Look for Plasmodium parasites.
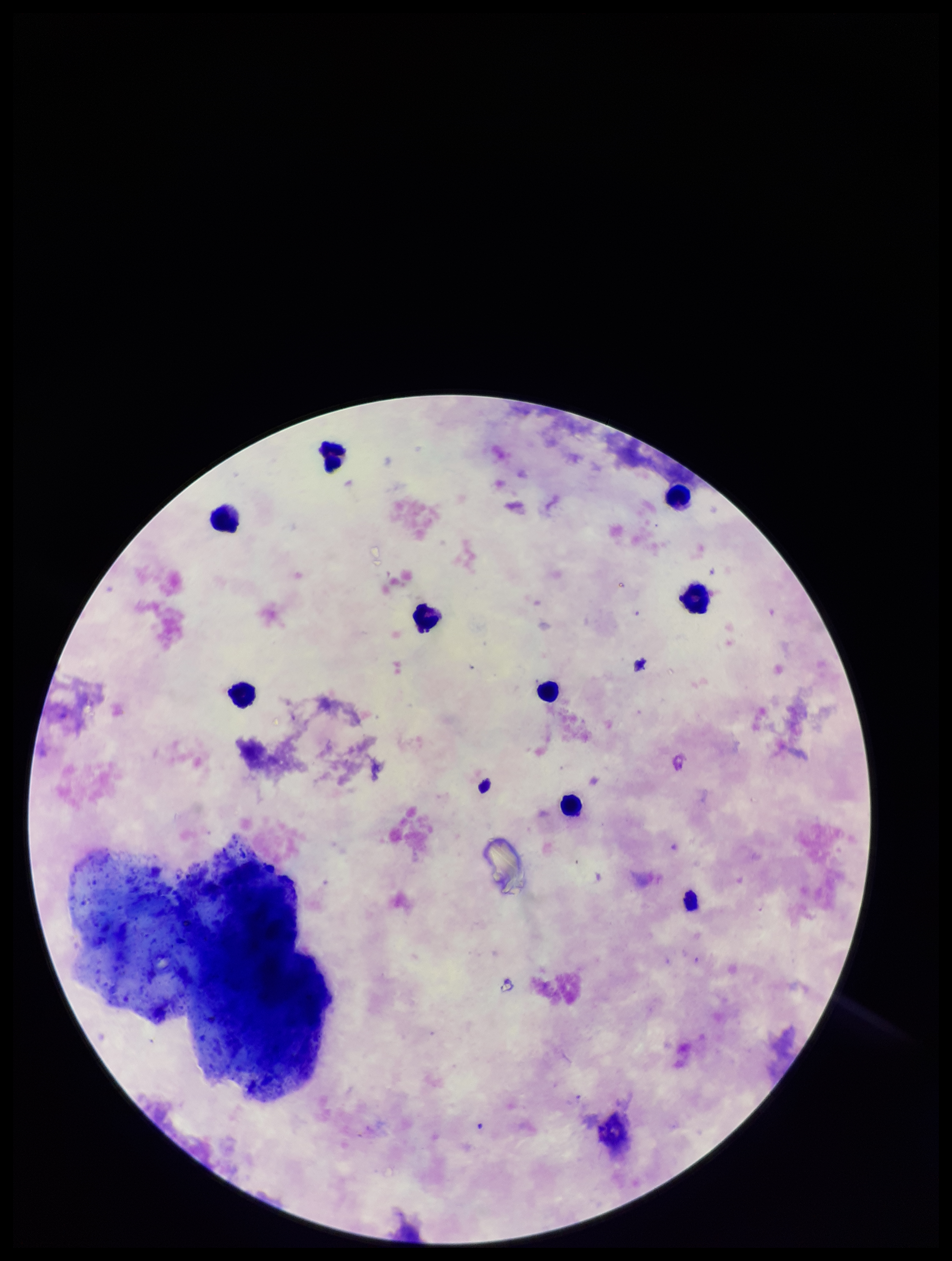

None seen.

{
  "preparation": "thick smear",
  "leukocyte_count": 8,
  "field_of_view": "one from this slide",
  "image_size": "952×1261 pixels",
  "parasite_count": 0,
  "patient_malaria_status": "negative",
  "stain": "Giemsa",
  "capture": "smartphone photograph through the microscope eyepiece"
}